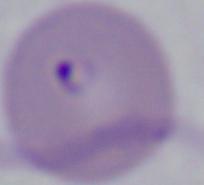
Summary:
  - Identification: Babesia
  - Magnification: 1000x
  - Modality: micrograph